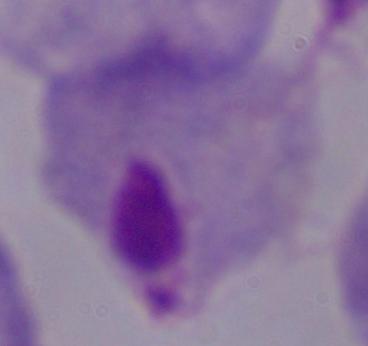

Summary:
  - Identification: trichomonad
  - Magnification: 1000x
  - Modality: micrograph